Locate every blood parasite and identify its species.
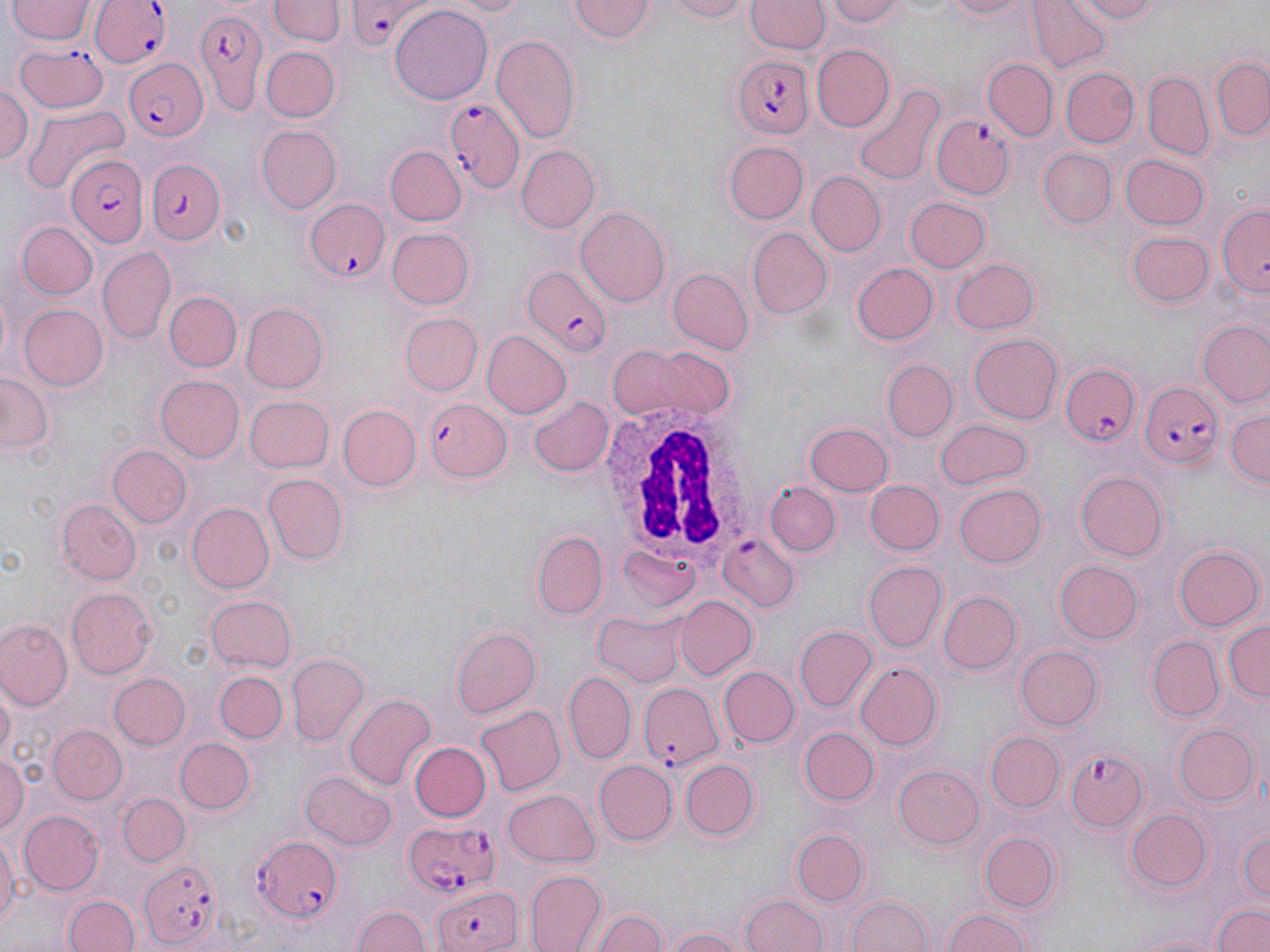
Approximate bounding boxes as (x1,y1)-(x2,y2) corner pairs in pixels.
Plasmodium falciparum-infected red blood cells (subset): (343,0)-(431,48), (190,3)-(270,112), (13,41)-(111,115), (734,54)-(812,140), (122,58)-(210,138), (445,96)-(524,194), (932,111)-(1015,201), (64,153)-(150,248), (145,158)-(226,247), (305,199)-(390,281), (520,268)-(615,354), (1057,356)-(1142,447), (1136,379)-(1222,465), (424,397)-(512,481), (718,535)-(798,613), (637,683)-(722,769), (1065,748)-(1148,831), (404,819)-(501,897), (247,834)-(345,922), (137,855)-(226,948), (432,882)-(523,952).
No Plasmodium ovale, Plasmodium malariae, Plasmodium vivax, Babesia divergens, or Trypanosoma brucei observed.

Summary:
  - White blood cell locations: (596,399)-(754,554)
  - Uninfected red blood cell locations (subset): (270,0)-(344,49), (434,0)-(536,19), (661,0)-(754,23), (745,0)-(828,56), (822,0)-(906,29), (930,0)-(1032,22), (1065,0)-(1170,25), (8,1)-(94,46), (567,1)-(655,45), (1029,1)-(1112,73), (390,6)-(491,102), (490,35)-(580,147), (812,44)-(895,132), (260,46)-(339,122), (983,58)-(1057,140), (1211,58)-(1268,141), (1062,67)-(1139,146), (1143,70)-(1213,159), (0,78)-(33,165), (854,83)-(946,187), (23,105)-(130,195), (254,125)-(341,213), (723,141)-(808,224), (385,144)-(466,227), (516,144)-(602,233), (1040,148)-(1116,229), (1121,154)-(1209,231), (807,172)-(887,257), (904,196)-(991,273), (1217,201)-(1269,296), (575,208)-(672,306), (16,221)-(97,298), (387,228)-(475,309), (748,228)-(831,319), (1126,229)-(1213,309), (98,246)-(176,346), (948,257)-(1039,336), (851,262)-(938,345), (667,268)-(753,354), (164,291)-(241,373), (17,301)-(108,392), (240,305)-(327,393), (400,313)-(483,395), (1197,317)-(1270,407), (481,329)-(571,419), (968,333)-(1063,425), (612,344)-(735,422), (883,358)-(957,440), (0,373)-(51,453), (154,375)-(244,462), (529,395)-(614,476), (245,396)-(335,473), (339,405)-(421,490), (1226,410)-(1269,484), (934,419)-(1032,489), (804,422)-(894,497), (107,445)-(193,529), (1074,470)-(1168,561), (264,473)-(348,565), (865,480)-(944,554), (951,481)-(1051,569), (764,482)-(841,558), (58,500)-(142,583), (185,501)-(274,594), (529,531)-(611,620), (1172,545)-(1261,632), (618,546)-(701,615), (864,560)-(948,651), (1056,560)-(1143,644), (66,588)-(158,679), (937,590)-(1020,675), (204,594)-(297,672), (675,597)-(757,680), (594,610)-(687,687), (0,618)-(72,707), (1223,620)-(1269,704), (451,626)-(542,718), (794,626)-(875,710), (1148,636)-(1223,721), (1016,645)-(1101,729), (287,653)-(370,744), (853,660)-(942,751), (718,666)-(798,747), (212,670)-(286,743), (563,671)-(636,763), (109,672)-(191,749), (0,685)-(13,765), (343,692)-(436,792), (475,704)-(565,797), (1173,723)-(1256,804), (47,724)-(127,804), (799,727)-(877,806), (985,733)-(1065,813), (175,736)-(254,813), (410,741)-(491,822), (0,751)-(27,836), (680,758)-(760,841), (596,759)-(679,844), (895,764)-(985,850), (300,770)-(396,852), (503,788)-(600,868), (119,792)-(190,866), (1125,806)-(1212,892), (20,809)-(105,895), (1238,826)-(1270,904), (0,827)-(20,939), (791,828)-(870,906), (979,831)-(1062,913), (523,867)-(606,951), (62,892)-(141,952), (738,893)-(828,952), (848,895)-(931,952), (1212,902)-(1270,952), (347,904)-(432,952), (590,906)-(668,952), (942,906)-(1035,952), (668,923)-(746,952), (1126,930)-(1232,951)
  - Slide-level diagnosis: Plasmodium falciparum
  - Image size: 1270×952 pixels
  - Modality: light microscopy
  - Preparation: thin blood film
  - Field of view: one of a larger specimen
  - Stain: May-Grünwald-Giemsa
  - Magnification: 1000x